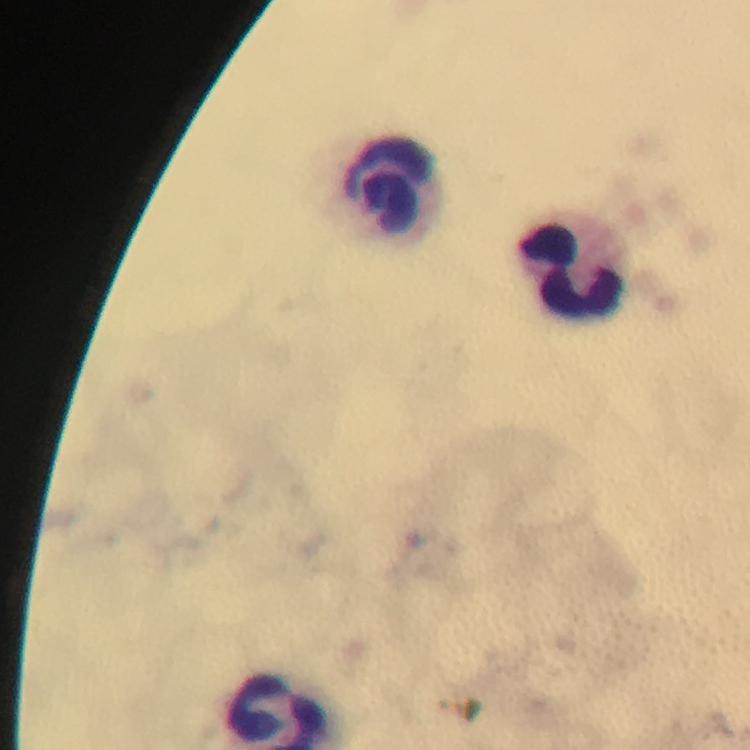

Approximate object centers, in pixels from the top-left corner.
Summary:
  - Leukocyte locations: (x=393, y=194), (x=574, y=267)
  - Stain: Giemsa
  - Preparation: thick blood smear
  - Magnification: 100x
  - Malaria parasites: none detected
  - Immersion oil: applied
  - Context: from a malaria diagnostic workup
  - Cropped from: a single field of view
  - Image size: 750×750 pixels
  - Capture: smartphone photograph through a microscope